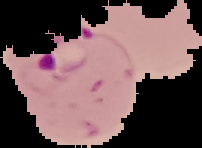

image size = 202×148 pixels
preparation = thin blood film
image type = segmented cell region with the area outside set to black
malaria status = parasitized